Point out every Plasmodium parasite and every leukocyte.
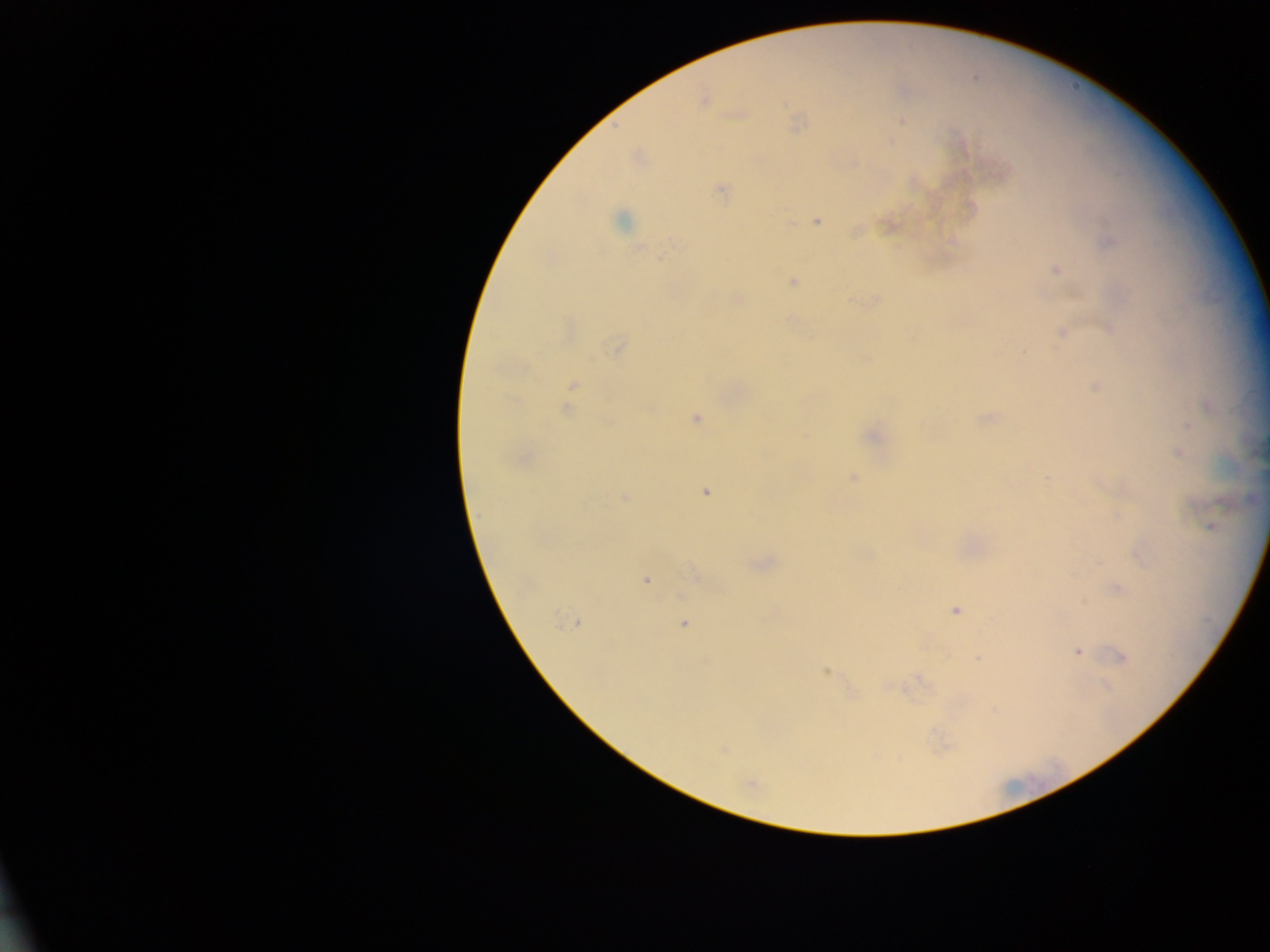

Approximate centers as x y in pixels.
Plasmodium parasites: 704 99; 901 121; 797 123; 638 157; 914 182; 720 189; 622 219; 817 220; 889 225; 1108 241; 640 246; 1056 269; 791 280; 735 298; 877 298; 1110 328; 1062 332; 617 346; 1095 387; 571 388; 568 404; 695 417; 983 419; 1187 423; 872 435; 1177 452; 520 459; 852 477; 1100 483; 705 492; 625 497; 1212 527; 1140 554; 760 564; 695 574; 645 578; 1116 588; 955 610; 572 622; 683 624; 1077 652; 1120 657; 979 659; 826 671; 1106 686; 722 748; 751 784.
No leukocytes observed.

Summary:
  - Preparation: thick blood film
  - Field of view: single
  - Capture: mobile-phone photograph through a microscope
  - Country: Ghana
  - Image size: 1270×952 pixels